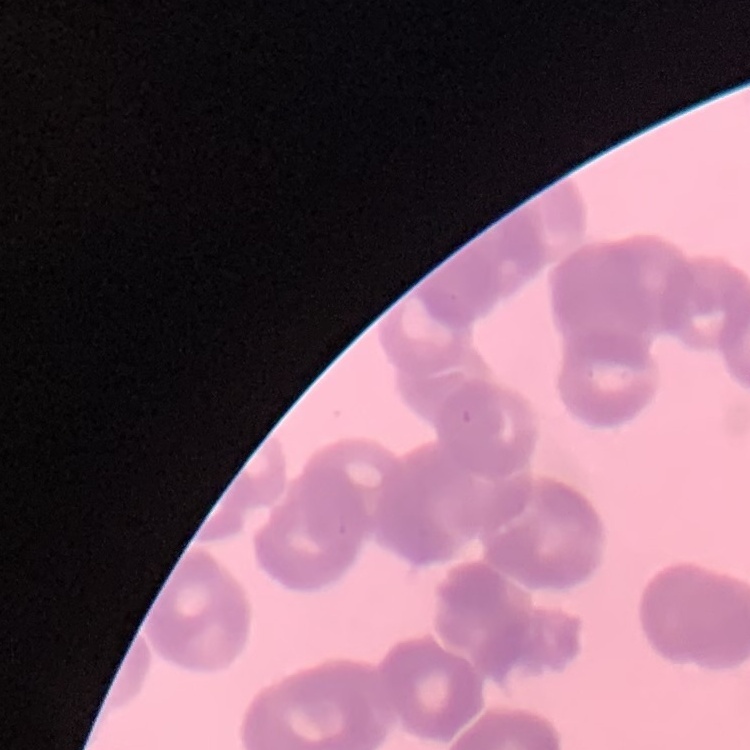

erythrocyte morphology = rouleaux formation
image type = square crop of a larger photomicrograph
preparation = thin blood film
stain = Field's or Giemsa